Report the malaria status of this cell.
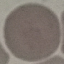

Uninfected.

capture = smartphone through the microscope eyepiece
image type = automatically extracted cell patch, resized to 64 × 64 pixels
stain = Giemsa
preparation = thin smear